Name the blood parasite species.
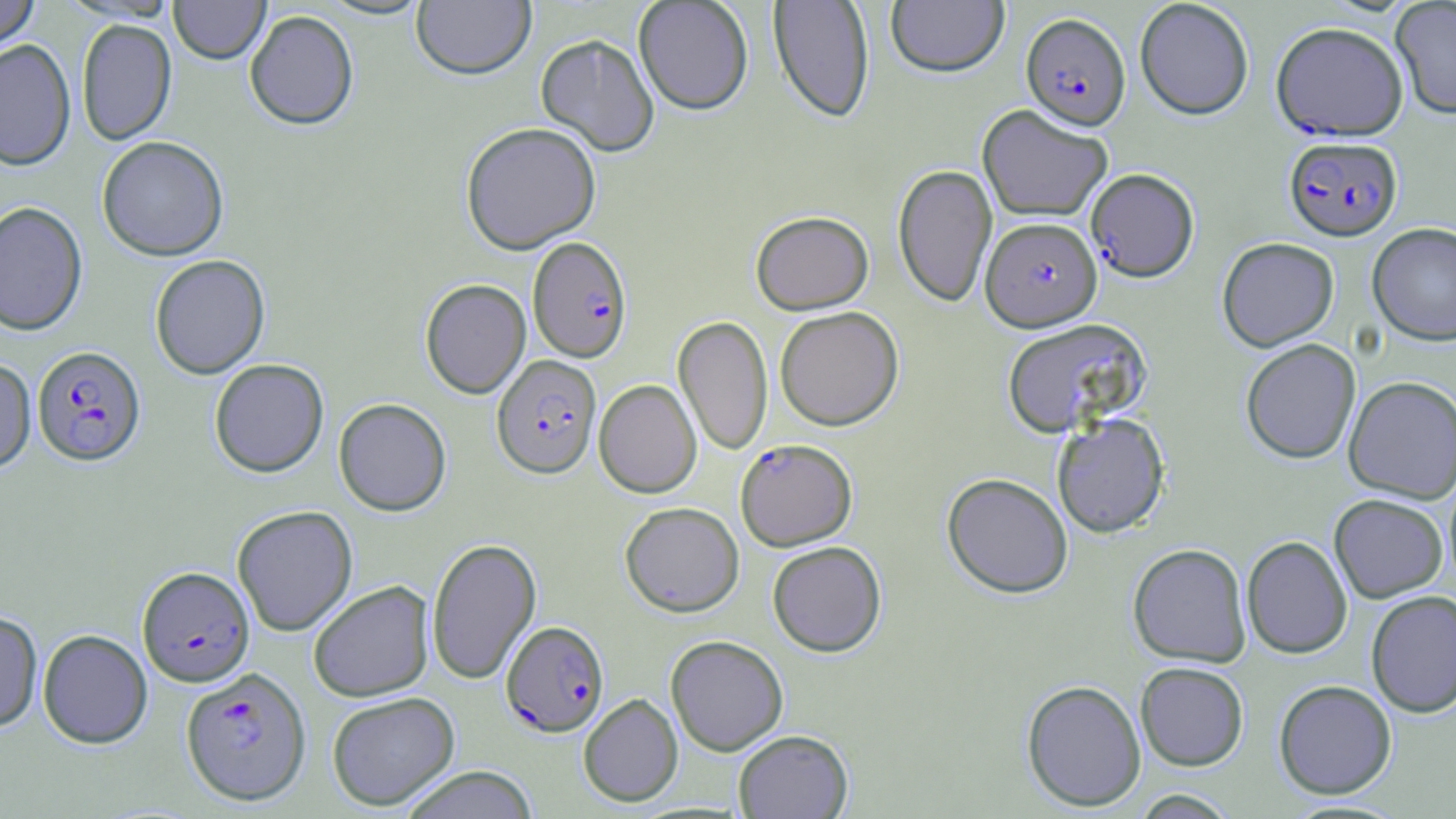

Plasmodium falciparum.

Summary:
  - Coordinate format: approximate bounding boxes as named x1/y1/x2/y2 corners in pixels
  - Plasmodium falciparum-infected red blood cell locations: (x1=1020, y1=15, x2=1131, y2=134), (x1=1271, y1=24, x2=1408, y2=143), (x1=1283, y1=137, x2=1403, y2=244), (x1=1086, y1=169, x2=1199, y2=284), (x1=981, y1=218, x2=1102, y2=333), (x1=528, y1=238, x2=633, y2=364), (x1=31, y1=347, x2=146, y2=469), (x1=491, y1=355, x2=602, y2=481), (x1=735, y1=440, x2=857, y2=551), (x1=137, y1=567, x2=255, y2=689), (x1=501, y1=621, x2=609, y2=738), (x1=181, y1=667, x2=311, y2=807)
  - Uninfected red blood cell locations: (x1=0, y1=0, x2=40, y2=58), (x1=169, y1=0, x2=270, y2=67), (x1=316, y1=0, x2=433, y2=21), (x1=412, y1=0, x2=536, y2=84), (x1=633, y1=0, x2=753, y2=117), (x1=768, y1=0, x2=875, y2=124), (x1=886, y1=0, x2=1009, y2=80), (x1=1135, y1=0, x2=1254, y2=122), (x1=1390, y1=0, x2=1456, y2=121), (x1=245, y1=12, x2=359, y2=134), (x1=77, y1=20, x2=177, y2=147), (x1=535, y1=35, x2=659, y2=159), (x1=0, y1=41, x2=76, y2=173), (x1=977, y1=105, x2=1113, y2=223), (x1=460, y1=123, x2=602, y2=256), (x1=97, y1=138, x2=228, y2=264), (x1=892, y1=165, x2=997, y2=308), (x1=0, y1=202, x2=88, y2=338), (x1=751, y1=211, x2=873, y2=315), (x1=1367, y1=224, x2=1456, y2=348), (x1=1217, y1=238, x2=1339, y2=353), (x1=150, y1=256, x2=270, y2=380), (x1=420, y1=279, x2=531, y2=400), (x1=775, y1=307, x2=904, y2=431), (x1=672, y1=315, x2=773, y2=456), (x1=1002, y1=319, x2=1151, y2=438), (x1=1241, y1=340, x2=1361, y2=465), (x1=209, y1=359, x2=329, y2=479), (x1=0, y1=360, x2=36, y2=476), (x1=1343, y1=377, x2=1456, y2=504), (x1=594, y1=380, x2=701, y2=499), (x1=334, y1=399, x2=451, y2=517), (x1=1052, y1=415, x2=1170, y2=538), (x1=942, y1=474, x2=1073, y2=599), (x1=1329, y1=495, x2=1447, y2=603), (x1=620, y1=502, x2=744, y2=618), (x1=232, y1=505, x2=358, y2=637), (x1=427, y1=537, x2=542, y2=686), (x1=1242, y1=537, x2=1352, y2=659), (x1=767, y1=541, x2=887, y2=658), (x1=1128, y1=544, x2=1251, y2=668), (x1=308, y1=581, x2=435, y2=703), (x1=1366, y1=590, x2=1456, y2=718), (x1=0, y1=611, x2=43, y2=733), (x1=38, y1=630, x2=153, y2=749), (x1=665, y1=635, x2=788, y2=756), (x1=1135, y1=662, x2=1249, y2=771), (x1=1021, y1=679, x2=1146, y2=811), (x1=1273, y1=680, x2=1397, y2=799), (x1=326, y1=692, x2=460, y2=811), (x1=578, y1=694, x2=683, y2=807), (x1=733, y1=730, x2=853, y2=818), (x1=398, y1=766, x2=541, y2=819), (x1=1128, y1=789, x2=1240, y2=818)
  - Preparation: thin blood film
  - Image size: 1456×819 pixels
  - Magnification: 1000x
  - Field of view: single
  - Modality: light microscopy
  - Stain: May-Grünwald-Giemsa